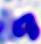
Summary:
  - Modality: photomicrograph
  - Magnification: 400x
  - Identification: leukocyte